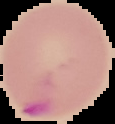

{
  "image_type": "cell region segmented out of the field of view; surrounding area masked to black",
  "image_size": "115×124 pixels",
  "preparation": "thin blood smear",
  "result": "Plasmodium parasites identified"
}